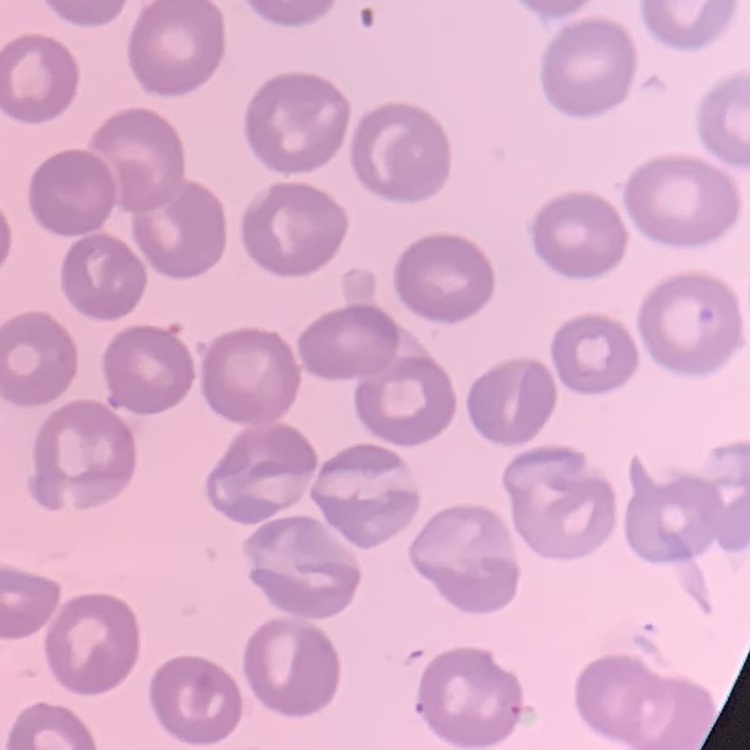

The erythrocytes exhibit no rouleaux formation. Stained with either Field's or Giemsa. One tile cut from a larger photomicrograph. Thin blood film.